Assess this cell for malaria.
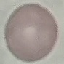
It is uninfected.

Cell patch, automatically extracted from a larger field of view and resized to 64 × 64 pixels. Giemsa-stained preparation. Acquired by smartphone through the microscope eyepiece. Thin blood film.